Name the cell type shown.
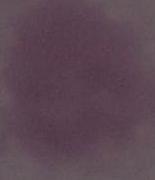
An erythrocyte.

{
  "magnification": "1000x",
  "modality": "photomicrograph"
}